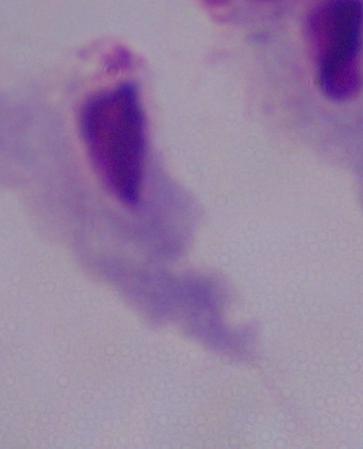
identification = trichomonad
magnification = 1000x
modality = micrograph